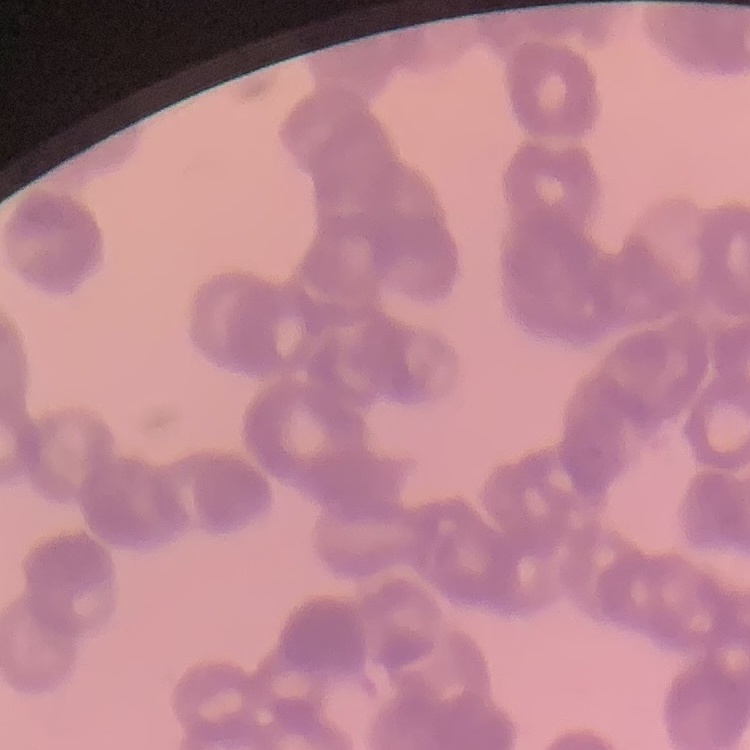

The erythrocytes exhibit rouleaux formation. Field's or Giemsa stain. Thin blood film. One tile cut from a larger photomicrograph.